Assess the morphology of the erythrocytes.
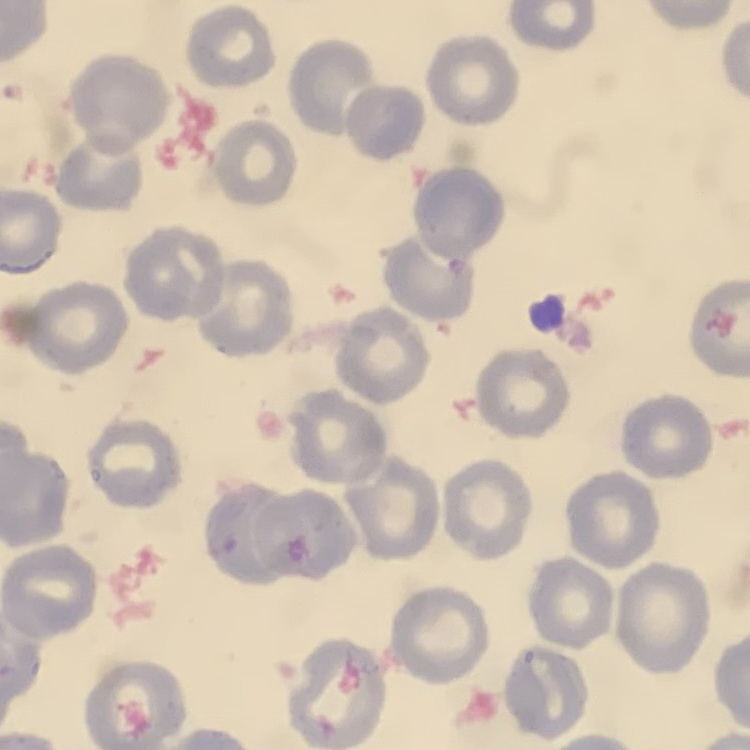

They show no rouleaux formation.

image type = one tile cut from a larger photomicrograph
stain = Field's or Giemsa
preparation = thin blood film